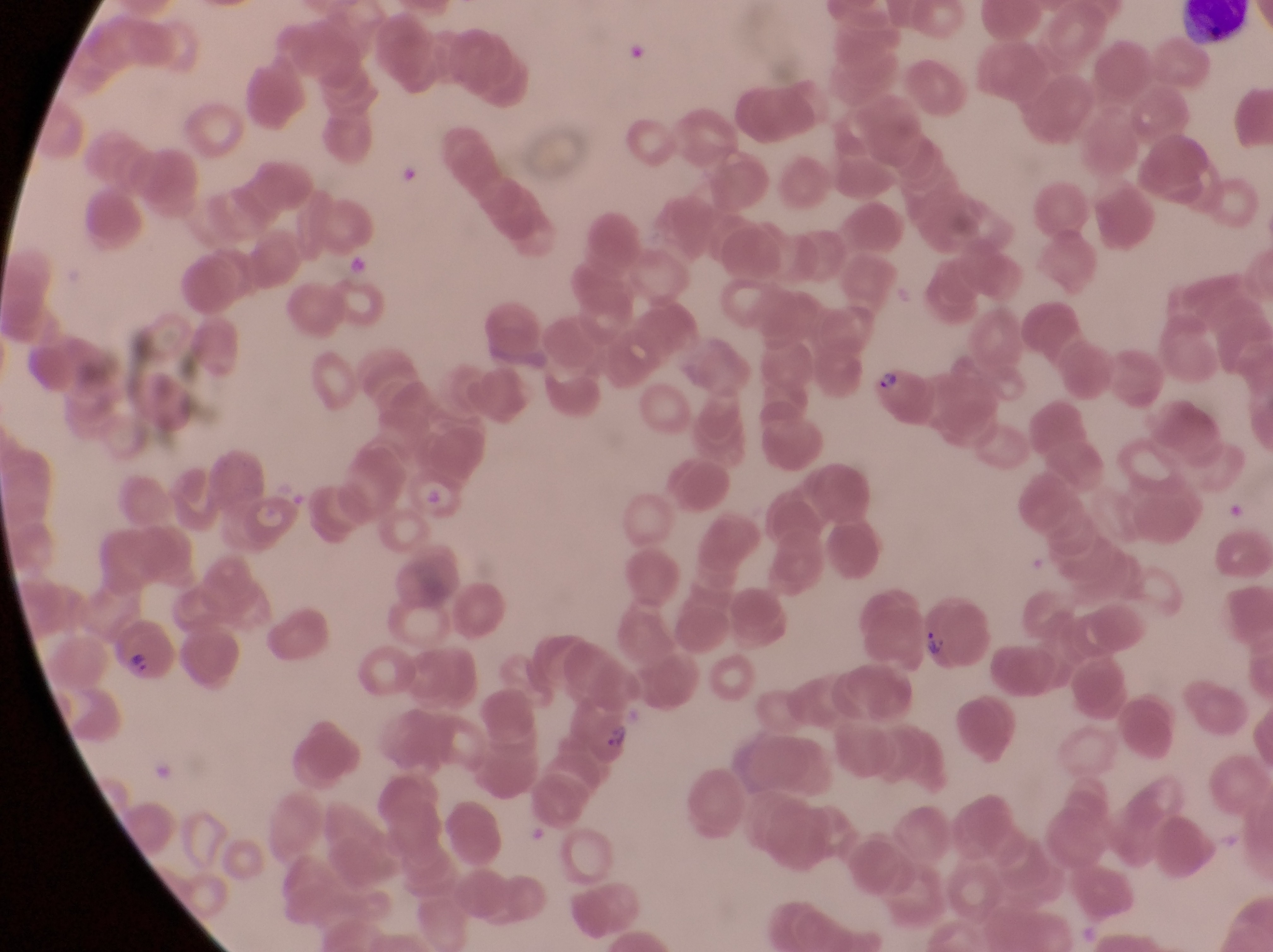

Approximate bounding boxes as (left, top, right, bottom) in pixels.
Summary:
  - Artifact (platelet-like body, stain precipitate, or debris) locations: (622, 32, 649, 63), (398, 164, 422, 188), (346, 256, 370, 276)
  - Leukocyte locations: (1175, 4, 1256, 45)
  - Parasitised red blood cell locations: (864, 360, 933, 430), (913, 596, 993, 668), (112, 632, 181, 692), (581, 703, 637, 772)
  - Capture: smartphone photograph through the eyepiece of an Olympus CX-23 microscope
  - Field of view: single
  - Magnification: 1000x
  - Preparation: thin blood film
  - Country: Uganda
  - Image size: 1273×952 pixels